Identify the parasite.
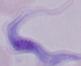

This is a trypanosome.

1000x magnification. Photomicrograph.